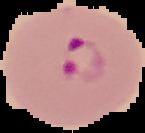
malaria_status: parasitized
image_type: cell region segmented out of the field of view; surrounding area masked to black
image_size: 145×133 pixels
preparation: thin blood smear